Describe the morphology of the erythrocytes.
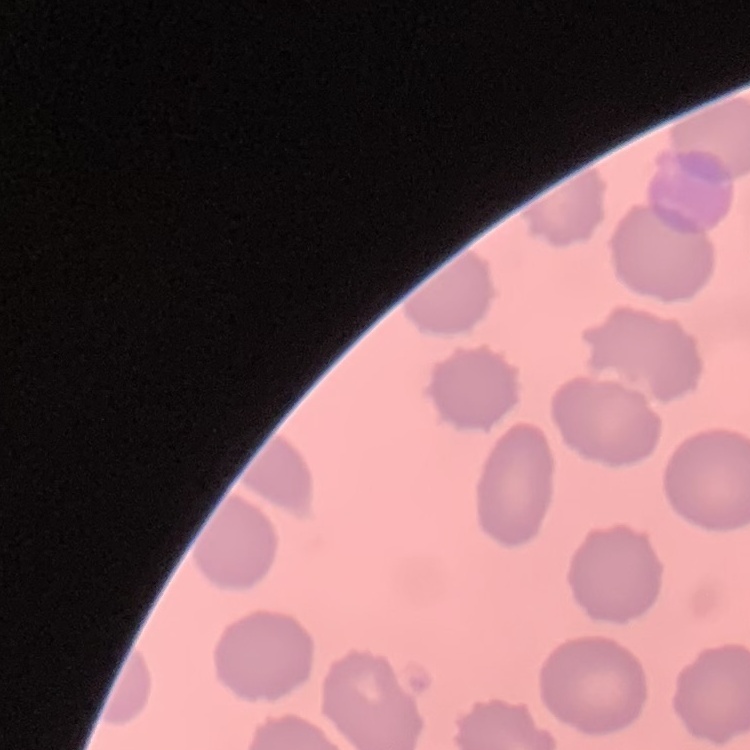
No rouleaux formation.

preparation = thin blood smear
image type = square crop of a larger photomicrograph
stain = Field's or Giemsa